Classify this cell by malaria status.
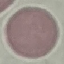
It is uninfected.

Giemsa stain. Cell patch, automatically extracted from a larger field of view and resized to 64 × 64 pixels. Photographed with a smartphone camera at the microscope eyepiece. Thin smear of blood.